Assess this cell for malaria.
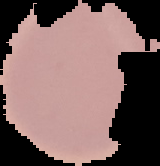

Uninfected.

Summary:
  - Image size: 160×166 pixels
  - Preparation: thin blood smear
  - Image type: segmented cell region with the area outside set to black